Assess the morphology of the red blood cells.
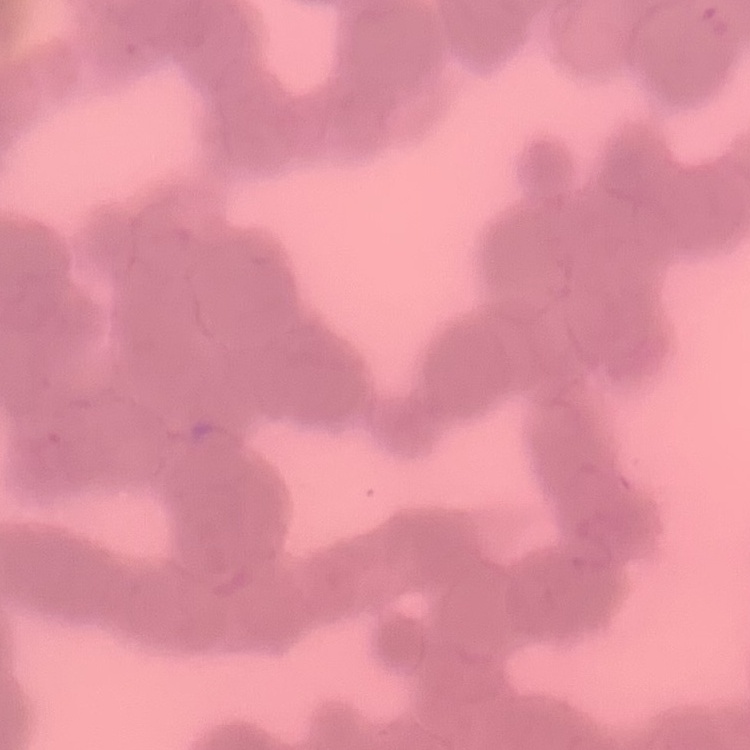
They show rouleaux formation.

stain = Field's or Giemsa
image type = one tile cut from a larger photomicrograph
preparation = thin blood smear